Comment on the morphology of the red blood cells.
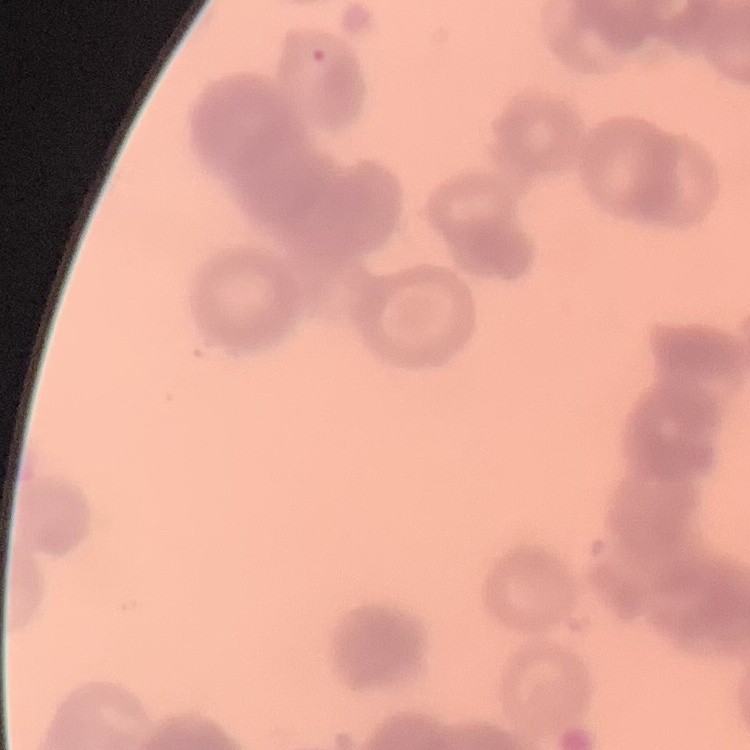

Rouleaux formation.

Summary:
  - Stain: Field's or Giemsa
  - Preparation: thin peripheral smear
  - Image type: one tile cut from a larger photomicrograph